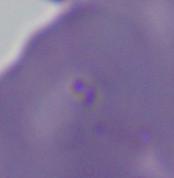
Summary:
  - Identification: Babesia
  - Modality: micrograph
  - Magnification: 1000x